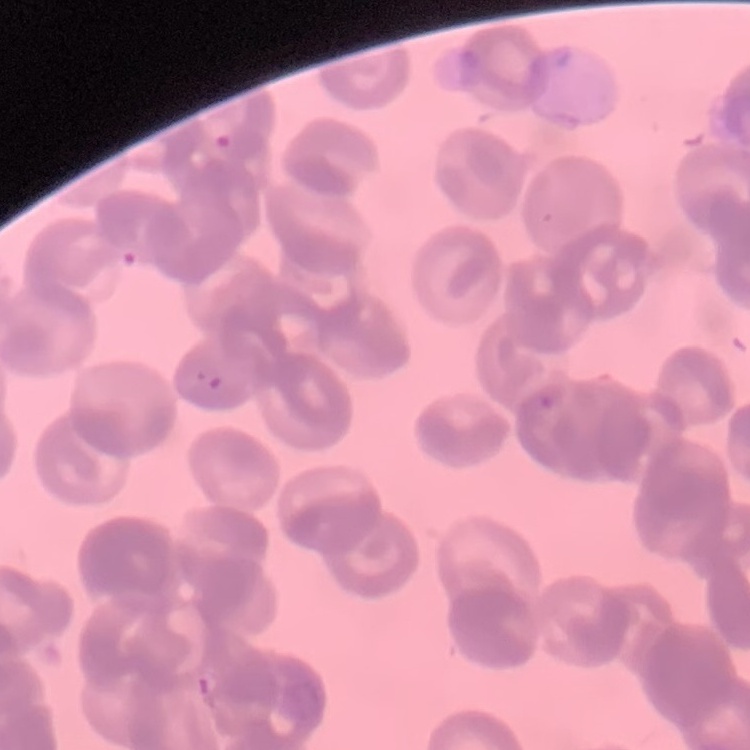
erythrocyte_morphology: rouleaux formation
preparation: thin blood film
image_type: square crop of a larger photomicrograph
stain: Field's or Giemsa